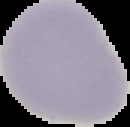 Result: negative for Plasmodium parasites. From a thin blood smear. The area outside the segmented cell region is set to black. Image is 130×127 pixels.